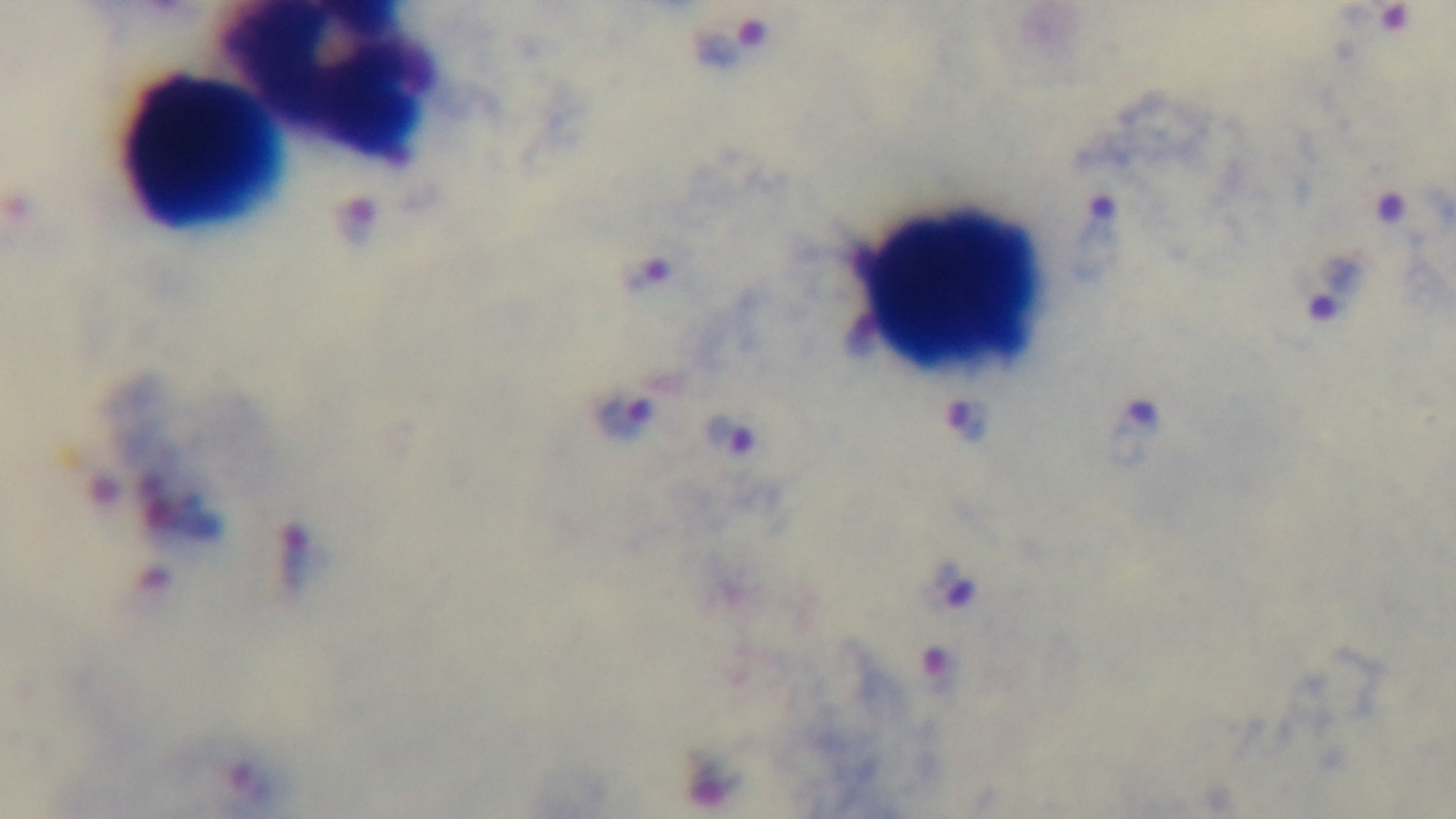

field_of_view: one from the slide
objective: 100x oil immersion
modality: light microscopy
stain: Giemsa
preparation: thick
malaria_status: infected
capture: mounted 4K digital camera